Assess this cell for malaria.
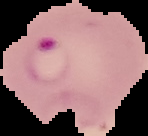
Parasitized.

From a thin blood film. Image is 148×136 pixels. Cell region segmented out of the field of view; the surrounding area is masked to black.